Assess this cell for malaria.
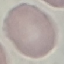
Uninfected.

preparation: thin blood film
image_type: cell patch, automatically extracted from a larger field of view and resized to 64 × 64 pixels
capture: smartphone camera at the microscope eyepiece
stain: Giemsa